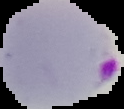 Cell region segmented out of the field of view; the surrounding area is masked to black. Image is 124×109 pixels. From a thin blood smear. Result: malaria parasites identified.